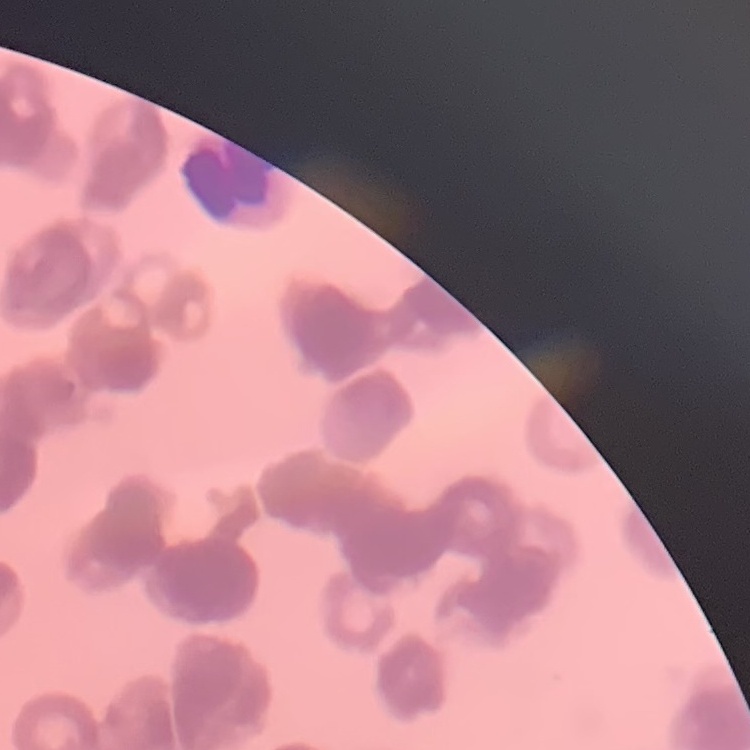

The erythrocytes show rouleaux formation. Stained with either Field's or Giemsa. Square crop of a larger photomicrograph. Thin blood film.